Locate every leukocyte (white blood cell).
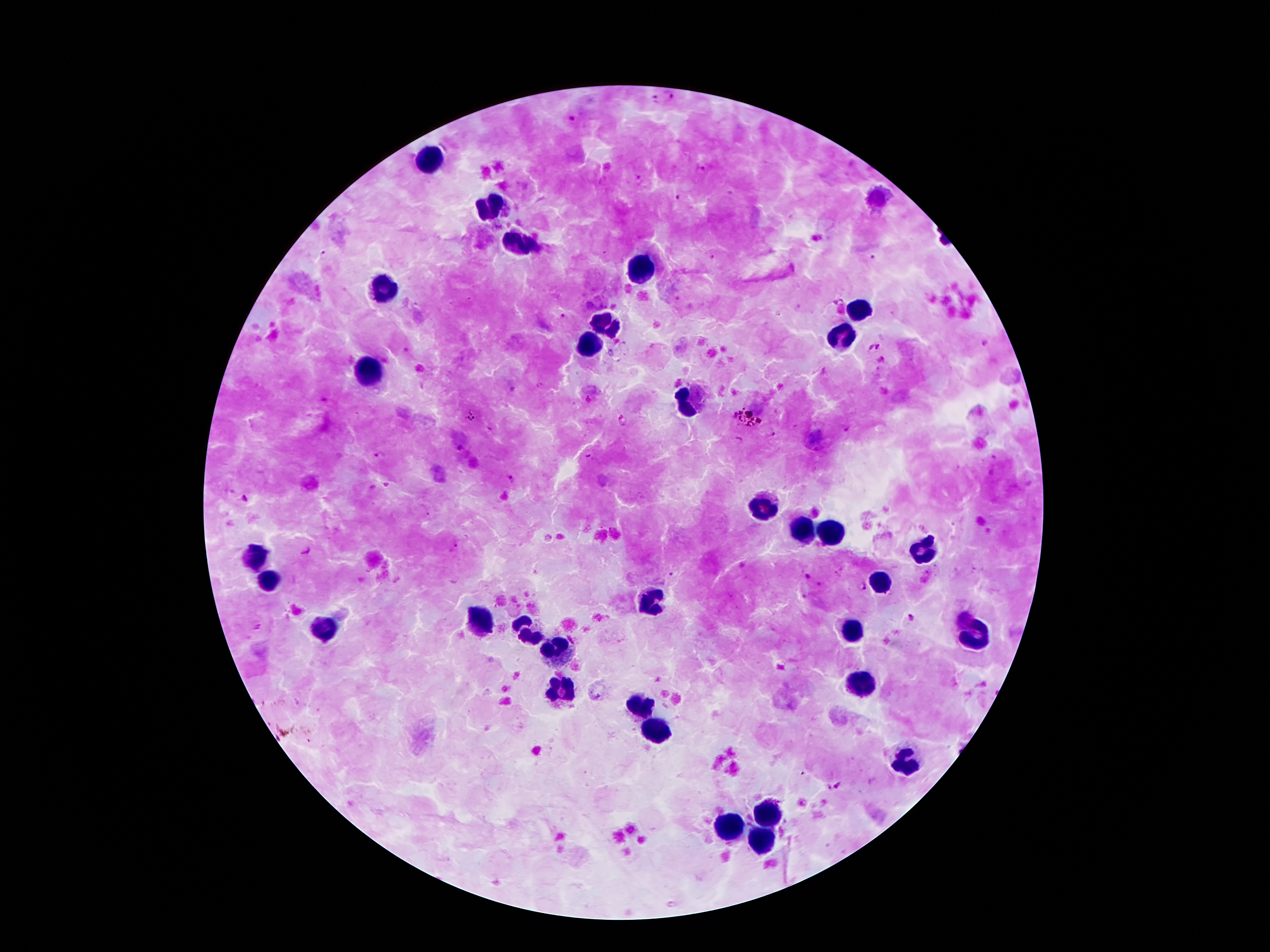
Approximate centers as {x, y} in pixels.
Leukocytes: {428, 160}, {489, 208}, {520, 242}, {646, 264}, {386, 284}, {859, 313}, {607, 325}, {839, 337}, {590, 344}, {369, 373}, {685, 406}, {761, 509}, {800, 533}, {831, 533}, {923, 549}, {252, 561}, {265, 578}, {881, 582}, {652, 603}, {480, 620}, {524, 630}, {850, 631}, {325, 633}, {974, 633}, {559, 650}, {858, 683}, {562, 686}, {637, 706}, {653, 727}, {908, 763}, {767, 814}, {725, 828}, {765, 842}.

{
  "preparation": "thick peripheral-blood smear",
  "capture": "smartphone through the microscope eyepiece",
  "image_size": "1270×952 pixels",
  "patient_malaria_status": "infected with Plasmodium falciparum",
  "field_of_view": "single",
  "plasmodium_parasite_locations": "approximate centers as {x, y} in pixels: {669, 97}, {654, 99}, {572, 118}, {700, 169}, {675, 197}, {324, 255}, {871, 256}, {711, 257}, {778, 314}, {564, 316}, {985, 342}, {879, 345}, {871, 348}, {882, 359}, {472, 415}, {771, 432}, {381, 456}, {587, 456}, {513, 480}, {245, 499}, {670, 574}, {807, 576}, {861, 585}, {911, 616}, {838, 786}",
  "magnification": "100x",
  "stain": "Giemsa"
}